Outline each Plasmodium falciparum-infected red blood cell.
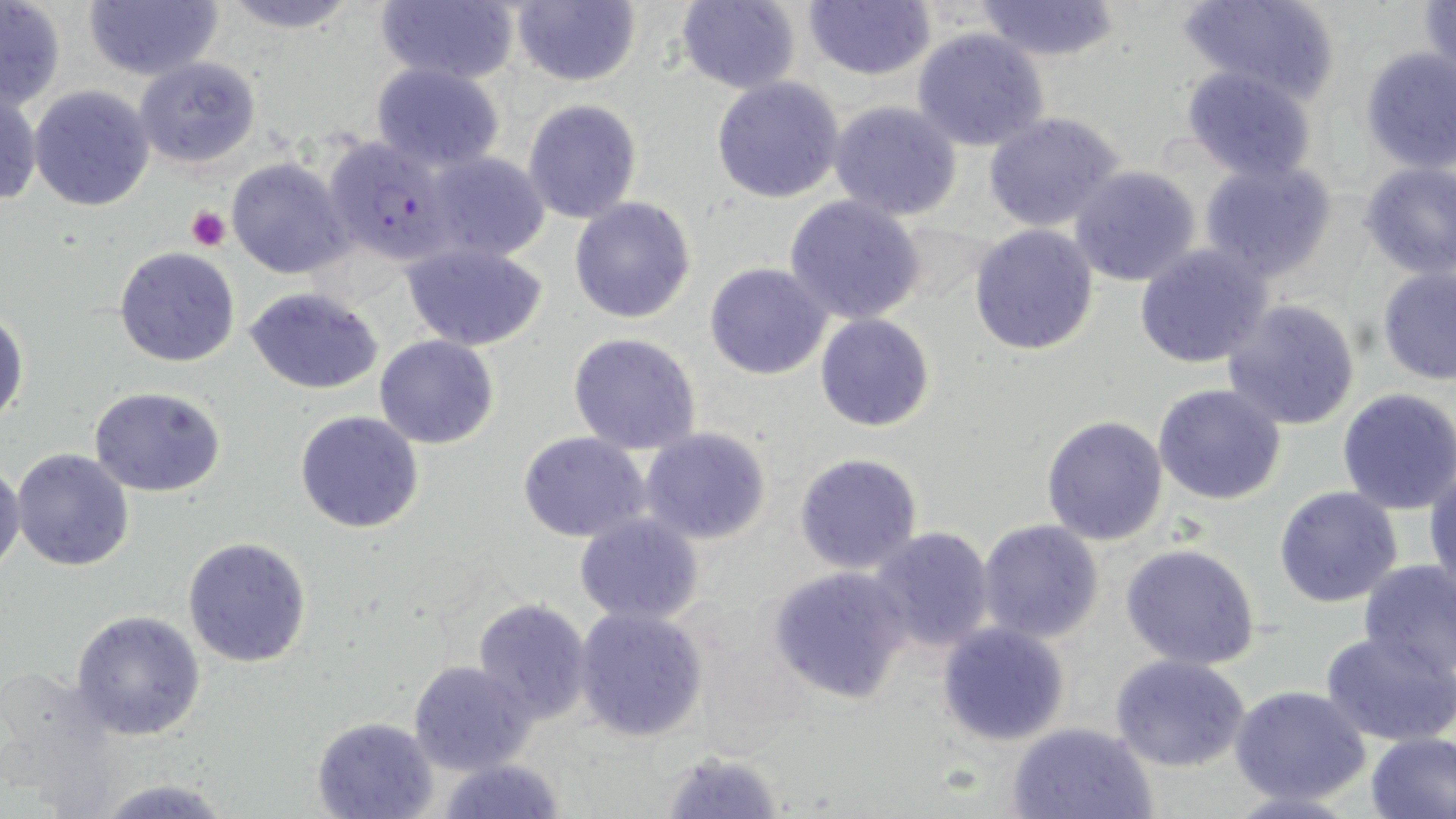

Approximate bounding boxes as (x1,y1)-(x2,y2) corner pairs in pixels.
Plasmodium falciparum-infected red blood cells: (322,133)-(456,268).

{
  "slide_level_diagnosis": "Plasmodium falciparum",
  "magnification": "1000x",
  "image_size": "1456×819 pixels",
  "stain": "May-Grünwald-Giemsa",
  "uninfected_red_blood_cell_locations": "approximate bounding boxes as (x1,y1)-(x2,y2) corner pairs in pixels: (0,0)-(68,110), (82,0)-(226,84), (213,0)-(365,32), (510,0)-(640,87), (677,0)-(801,95), (1175,0)-(1338,102), (1419,0)-(1455,89), (372,1)-(519,87), (802,1)-(936,82), (974,1)-(1123,61), (912,29)-(1051,153), (1358,46)-(1456,173), (134,56)-(261,170), (371,62)-(507,174), (1179,66)-(1320,185), (711,77)-(846,204), (29,84)-(157,212), (0,87)-(41,209), (523,99)-(643,223), (827,100)-(963,221), (982,112)-(1124,233), (422,151)-(553,264), (226,157)-(353,280), (1197,158)-(1338,283), (1358,161)-(1455,279), (1069,164)-(1203,286), (784,195)-(925,324), (568,196)-(696,323), (968,223)-(1099,356), (401,240)-(550,351), (1133,245)-(1275,369), (115,247)-(239,367), (702,263)-(833,381), (1378,266)-(1456,385), (245,287)-(384,394), (1220,298)-(1362,430), (0,305)-(28,432), (814,312)-(937,432), (567,331)-(703,455), (373,334)-(500,450), (1152,382)-(1287,505), (88,387)-(227,495), (1335,389)-(1456,515), (294,410)-(425,534), (1041,414)-(1169,545), (640,426)-(773,545), (517,432)-(652,543), (11,448)-(135,572), (793,452)-(924,574), (0,458)-(24,573), (1426,461)-(1456,601), (1274,485)-(1403,607), (573,513)-(704,626), (977,518)-(1106,644), (867,527)-(997,654), (182,536)-(312,668), (1120,542)-(1261,670), (1358,559)-(1456,683), (767,565)-(913,705), (471,600)-(593,723), (574,606)-(710,742), (70,610)-(205,740), (937,622)-(1069,748), (1321,631)-(1455,746), (1111,655)-(1252,772), (408,659)-(536,776), (1229,685)-(1372,805), (312,716)-(437,819), (1007,721)-(1158,818), (1364,732)-(1456,819), (655,748)-(784,817), (433,757)-(571,817), (91,776)-(236,817)",
  "modality": "light microscopy",
  "field_of_view": "one of a larger specimen",
  "platelet_locations": "approximate bounding boxes as (x1,y1)-(x2,y2) corner pairs in pixels: (186,205)-(230,251)",
  "preparation": "thin blood film"
}